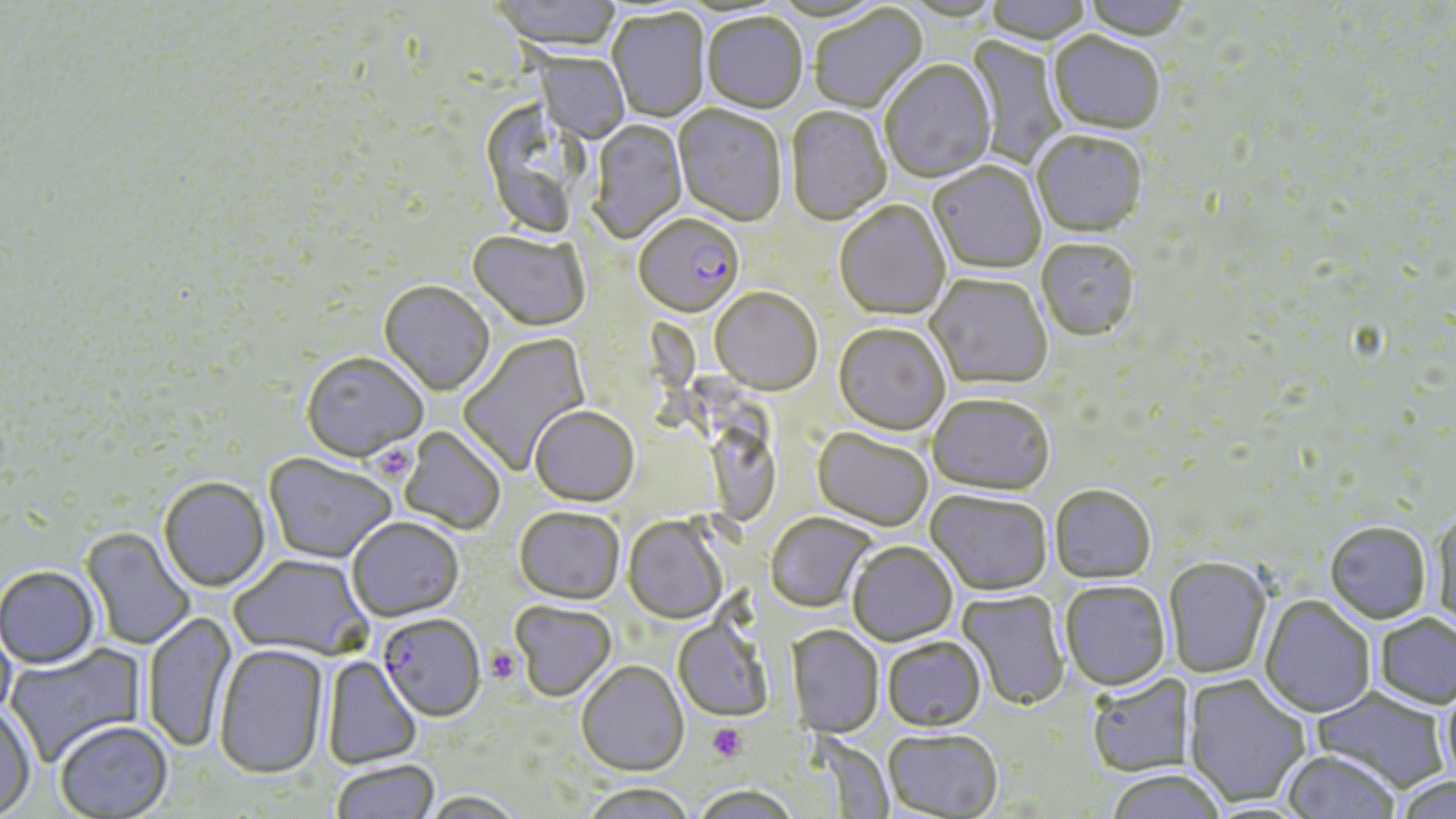

Summary:
  - Coordinate format: approximate bounding boxes as (x1, y1, x2, y2) in pixels
  - Platelet locations: (370, 444, 416, 483), (485, 646, 522, 683), (707, 723, 747, 762)
  - Uninfected red blood cell locations: (489, 0, 622, 55), (985, 0, 1092, 46), (1081, 0, 1194, 43), (810, 6, 928, 115), (607, 10, 710, 123), (702, 14, 807, 115), (1048, 34, 1165, 137), (962, 35, 1066, 168), (534, 53, 629, 144), (880, 61, 997, 185), (672, 107, 787, 229), (786, 108, 891, 227), (591, 120, 687, 243), (1031, 133, 1148, 238), (928, 163, 1046, 275), (834, 202, 951, 321), (468, 232, 589, 332), (1036, 239, 1140, 341), (927, 273, 1053, 390), (379, 282, 494, 397), (710, 289, 823, 396), (834, 323, 951, 435), (458, 332, 591, 477), (301, 351, 428, 462), (928, 392, 1054, 495), (529, 405, 639, 506), (400, 426, 506, 535), (812, 427, 933, 531), (263, 452, 397, 564), (158, 476, 270, 591), (1049, 484, 1157, 583), (926, 489, 1053, 596), (514, 506, 625, 603), (1431, 510, 1456, 631), (765, 512, 876, 611), (347, 516, 464, 621), (622, 516, 728, 625), (1325, 521, 1431, 623), (80, 527, 196, 651), (847, 541, 957, 645), (230, 554, 371, 661), (1164, 557, 1271, 679), (0, 564, 100, 669), (1060, 580, 1171, 691), (958, 590, 1069, 710), (1259, 595, 1375, 718), (510, 601, 616, 702), (141, 610, 237, 753), (1374, 612, 1456, 709), (673, 619, 773, 721), (0, 621, 17, 724), (787, 625, 884, 738), (882, 636, 986, 731), (4, 643, 147, 769), (214, 644, 329, 778), (321, 656, 421, 770), (576, 660, 688, 776), (1086, 673, 1195, 778), (1184, 674, 1312, 809), (1441, 679, 1456, 789), (1310, 687, 1451, 793), (0, 705, 36, 817), (54, 720, 172, 818), (883, 728, 1003, 818), (1281, 750, 1401, 818), (331, 758, 439, 819), (1104, 769, 1227, 819), (1393, 775, 1456, 819), (580, 781, 697, 819), (691, 784, 800, 819), (423, 791, 525, 818)
  - Plasmodium falciparum-infected red blood cell locations: (633, 216, 744, 319), (379, 613, 486, 721)
  - Slide-level diagnosis: Plasmodium falciparum
  - Preparation: thin blood film
  - Modality: light microscopy
  - Image size: 1456×819 pixels
  - Magnification: 1000x
  - Stain: May-Grünwald-Giemsa
  - Field of view: one of a larger specimen